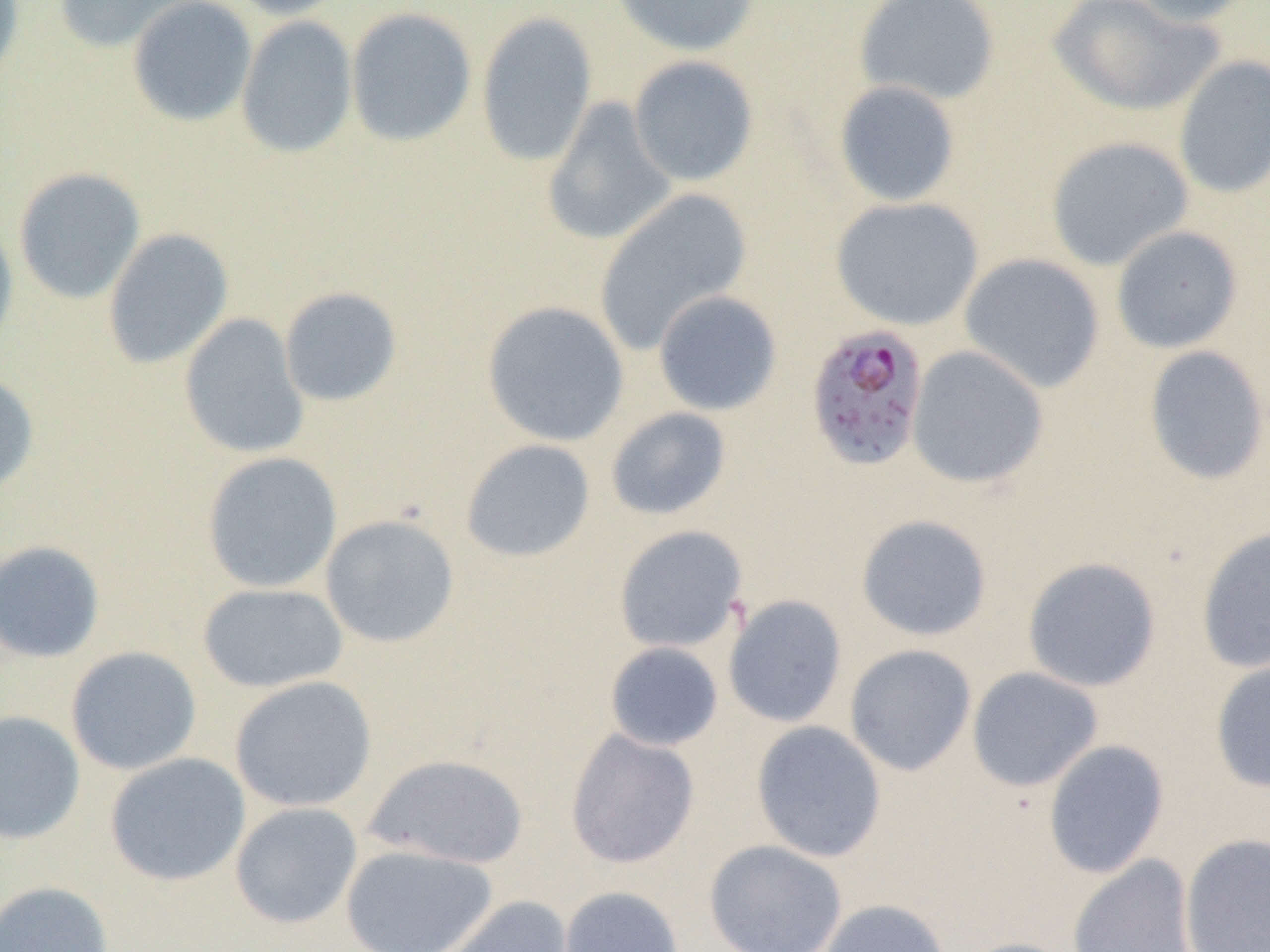

Summary:
  - Coordinate format: approximate bounding boxes as named x1/y1/x2/y2 corners in pixels
  - Uninfected red blood cell locations: (x1=53, y1=0, x2=203, y2=54), (x1=127, y1=0, x2=258, y2=127), (x1=224, y1=0, x2=352, y2=20), (x1=609, y1=0, x2=762, y2=57), (x1=853, y1=0, x2=1001, y2=106), (x1=1047, y1=0, x2=1225, y2=117), (x1=1122, y1=0, x2=1260, y2=26), (x1=0, y1=1, x2=25, y2=96), (x1=345, y1=7, x2=477, y2=147), (x1=475, y1=11, x2=598, y2=166), (x1=236, y1=15, x2=357, y2=158), (x1=628, y1=55, x2=759, y2=186), (x1=1172, y1=55, x2=1270, y2=199), (x1=833, y1=80, x2=961, y2=207), (x1=541, y1=96, x2=678, y2=247), (x1=1045, y1=136, x2=1194, y2=271), (x1=13, y1=167, x2=146, y2=305), (x1=593, y1=189, x2=753, y2=354), (x1=830, y1=196, x2=984, y2=331), (x1=0, y1=218, x2=19, y2=359), (x1=1111, y1=225, x2=1243, y2=353), (x1=103, y1=227, x2=234, y2=369), (x1=959, y1=253, x2=1105, y2=393), (x1=279, y1=287, x2=403, y2=407), (x1=653, y1=289, x2=783, y2=416), (x1=481, y1=301, x2=630, y2=447), (x1=179, y1=313, x2=309, y2=459), (x1=907, y1=344, x2=1049, y2=489), (x1=1143, y1=345, x2=1270, y2=486), (x1=0, y1=371, x2=39, y2=496), (x1=605, y1=406, x2=733, y2=521), (x1=460, y1=439, x2=596, y2=563), (x1=201, y1=451, x2=343, y2=594), (x1=320, y1=514, x2=460, y2=648), (x1=855, y1=514, x2=992, y2=641), (x1=613, y1=525, x2=749, y2=654), (x1=1196, y1=526, x2=1270, y2=673), (x1=0, y1=540, x2=106, y2=663), (x1=1022, y1=556, x2=1161, y2=692), (x1=198, y1=583, x2=349, y2=693), (x1=722, y1=594, x2=847, y2=728), (x1=604, y1=642, x2=724, y2=752), (x1=844, y1=644, x2=977, y2=776), (x1=65, y1=645, x2=202, y2=776), (x1=1209, y1=655, x2=1270, y2=793), (x1=967, y1=666, x2=1103, y2=791), (x1=229, y1=675, x2=377, y2=812), (x1=0, y1=710, x2=85, y2=845), (x1=750, y1=720, x2=887, y2=863), (x1=565, y1=728, x2=700, y2=869), (x1=1042, y1=739, x2=1170, y2=879), (x1=104, y1=752, x2=251, y2=886), (x1=363, y1=753, x2=529, y2=869), (x1=230, y1=802, x2=363, y2=929), (x1=1180, y1=833, x2=1270, y2=952), (x1=703, y1=839, x2=848, y2=952), (x1=340, y1=843, x2=498, y2=952), (x1=1068, y1=854, x2=1198, y2=952), (x1=0, y1=881, x2=114, y2=952), (x1=558, y1=886, x2=684, y2=952), (x1=438, y1=895, x2=577, y2=952), (x1=817, y1=898, x2=950, y2=952), (x1=955, y1=937, x2=1082, y2=952)
  - Plasmodium falciparum-infected red blood cell locations: (x1=805, y1=322, x2=930, y2=471)
  - Slide-level diagnosis: Plasmodium falciparum
  - Magnification: 1000x
  - Field of view: one of a larger specimen
  - Modality: light microscopy
  - Preparation: thin blood film
  - Image size: 1270×952 pixels